Report the malaria status of this cell.
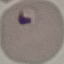
Parasitized.

Summary:
  - Image type: automatically extracted cell patch, resized to 64 × 64 pixels
  - Preparation: thin smear
  - Stain: Giemsa
  - Capture: smartphone camera at the microscope eyepiece